Describe the morphology of the erythrocytes.
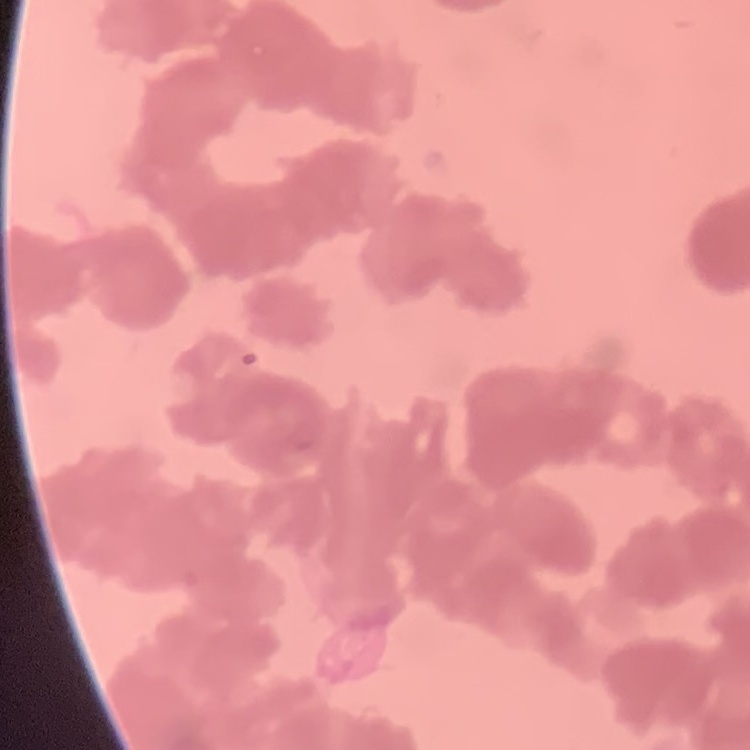

They show rouleaux formation.

Field's or Giemsa stain. Thin peripheral smear. One tile cut from a larger photomicrograph.